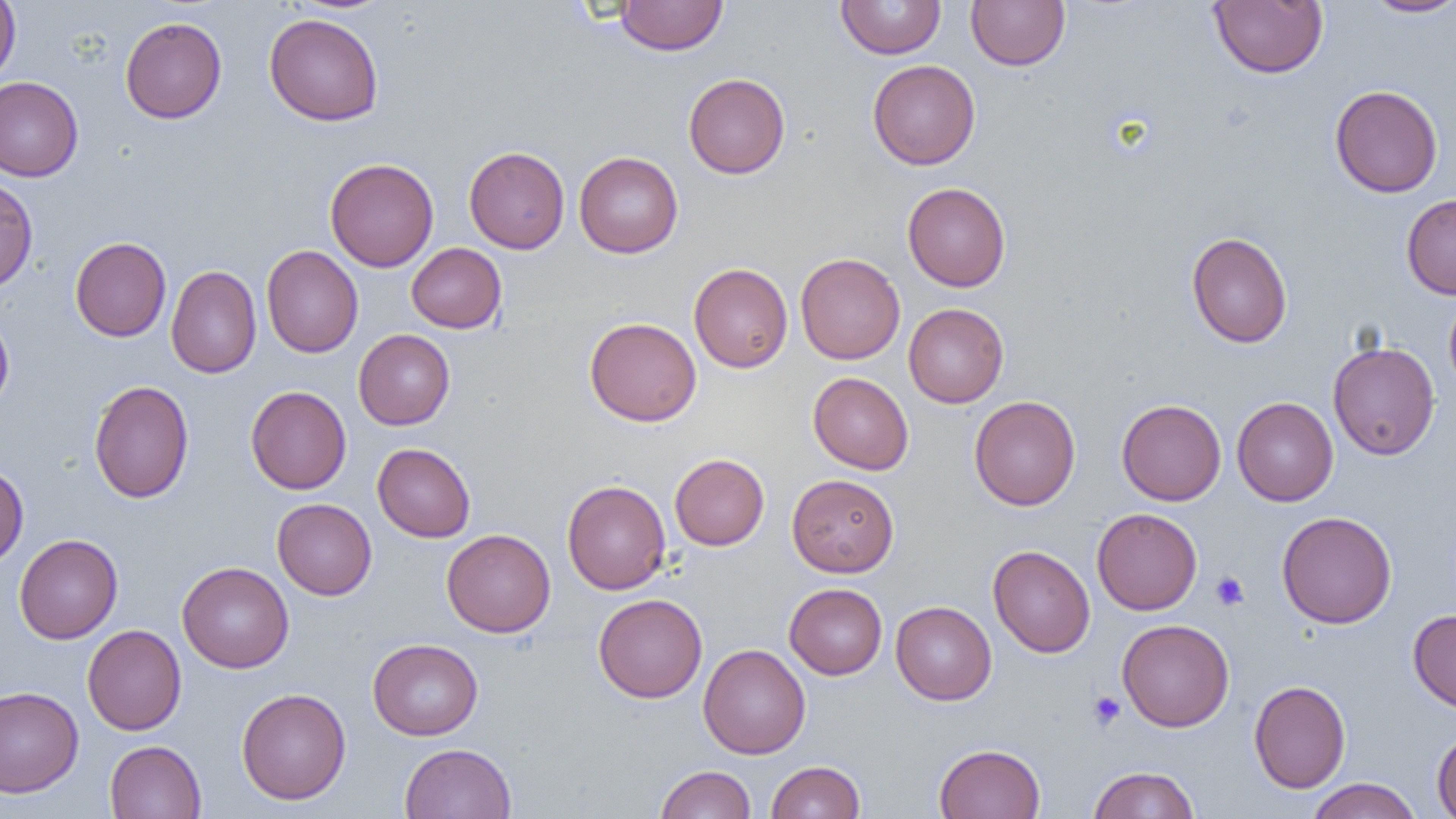

Approximate bounding boxes as (x1, y1, x2, y2) in pixels. Uninfected red blood cell locations: (0, 0, 20, 84), (615, 0, 727, 55), (836, 0, 946, 59), (966, 0, 1070, 71), (1361, 0, 1456, 18), (1209, 1, 1328, 78), (264, 12, 384, 126), (120, 16, 227, 123), (868, 59, 981, 170), (683, 73, 790, 179), (0, 77, 83, 182), (1329, 84, 1443, 198), (464, 147, 569, 253), (574, 151, 684, 258), (324, 157, 439, 272), (0, 177, 38, 293), (902, 182, 1011, 291), (1401, 194, 1456, 299), (1186, 232, 1293, 348), (70, 236, 171, 342), (406, 243, 507, 333), (261, 245, 363, 358), (796, 253, 905, 364), (689, 263, 793, 373), (166, 265, 262, 378), (1444, 292, 1456, 398), (903, 303, 1009, 408), (0, 307, 14, 414), (585, 317, 701, 426), (353, 329, 455, 430), (1327, 340, 1440, 460), (808, 372, 914, 475), (88, 380, 194, 503), (245, 386, 351, 494), (968, 395, 1081, 510), (1232, 397, 1338, 506), (1116, 399, 1226, 505), (372, 443, 475, 542), (669, 453, 769, 550), (0, 463, 29, 567), (786, 473, 899, 577), (562, 480, 671, 595), (272, 498, 377, 600), (1091, 507, 1202, 615), (1277, 511, 1397, 629), (442, 529, 556, 637), (14, 534, 122, 643), (988, 544, 1095, 657), (177, 561, 294, 673), (785, 583, 887, 679), (593, 594, 707, 703), (890, 601, 997, 705), (1408, 609, 1456, 713), (1117, 618, 1234, 732), (83, 624, 186, 735), (368, 638, 483, 740), (698, 644, 810, 759), (1249, 680, 1350, 793), (0, 686, 84, 797), (236, 687, 351, 804), (1432, 727, 1456, 819), (105, 740, 206, 818), (400, 742, 517, 819), (934, 743, 1046, 819), (766, 761, 865, 819), (655, 765, 756, 819), (1088, 765, 1199, 818), (1306, 778, 1422, 819). Platelet locations: (1211, 571, 1249, 611), (1087, 691, 1125, 731). Slide-level diagnosis: no evidence of blood parasites. Single field of view. Thin blood smear. Optical microscopy. Captured at 1000x magnification. Image is 1456×819 pixels.